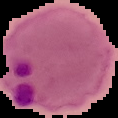
Summary:
  - Malaria status: parasitized
  - Image size: 118×118 pixels
  - Image type: segmented cell region on a black background
  - Preparation: thin blood film